State which cell type is depicted.
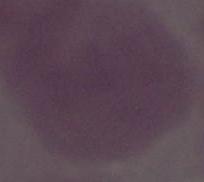

This is an erythrocyte.

Captured at 1000x magnification. Photomicrograph.